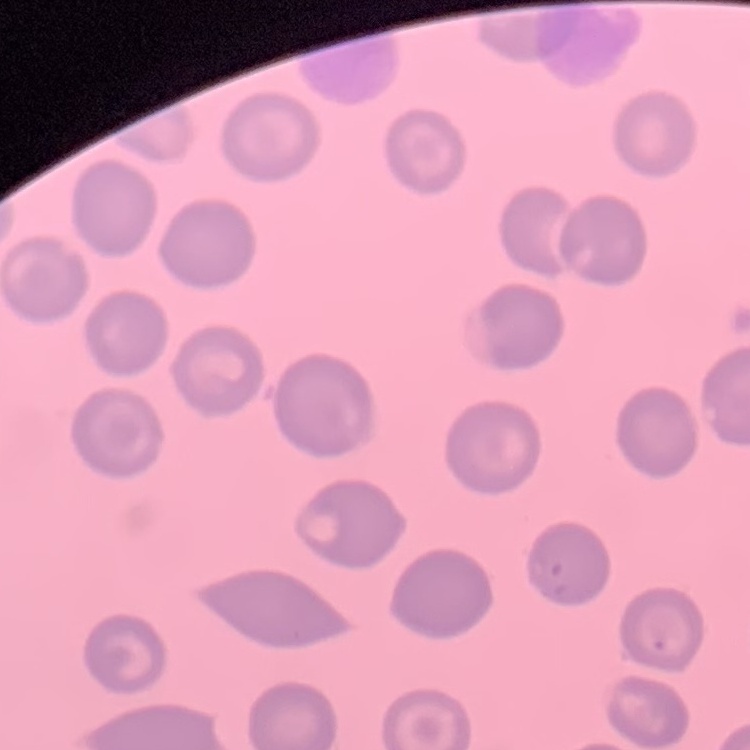

The erythrocytes exhibit no rouleaux formation. Field's or Giemsa stain. Square crop of a larger photomicrograph. Thin peripheral smear.